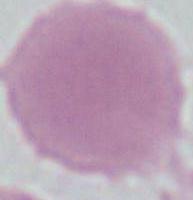
Summary:
  - Magnification: 1000x
  - Modality: photomicrograph
  - Identification: red blood cell